Identify the parasite.
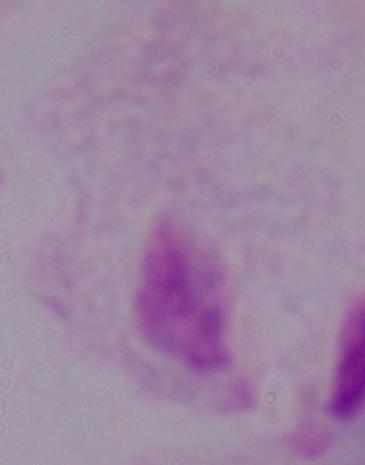
This is a trichomonad.

Photomicrograph. 1000x magnification.